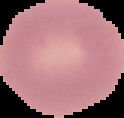

malaria status = uninfected
image size = 124×118 pixels
image type = segmented cell region on a black background
preparation = thin blood smear